Outline each Plasmodium ovale-infected red blood cell.
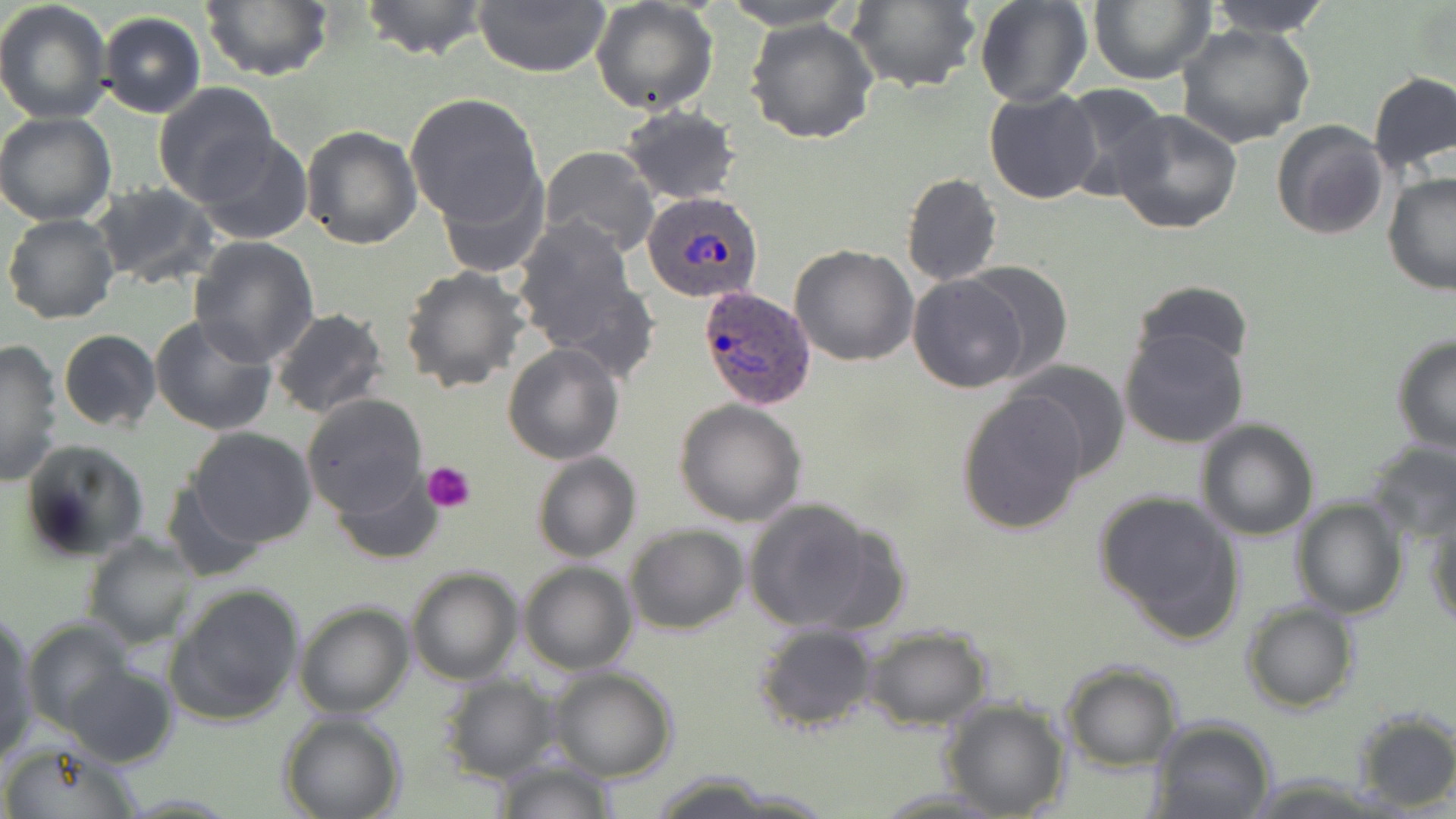

Approximate bounding boxes as [x1, y1, x2, y2] in pixels.
Plasmodium ovale-infected red blood cells: [642, 188, 766, 305], [699, 285, 818, 411].

slide_level_diagnosis: Plasmodium ovale
stain: May-Grünwald-Giemsa
image_size: 1456×819 pixels
modality: optical microscopy
uninfected_red_blood_cell_locations: 'approximate bounding boxes as [x1, y1, x2, y2] in pixels: [0, 0, 114, 125], [358, 0, 492, 60], [471, 0, 611, 76], [716, 0, 861, 29], [846, 0, 981, 93], [974, 0, 1091, 107], [1086, 0, 1215, 86], [1201, 0, 1336, 39], [200, 1, 333, 82], [590, 1, 719, 115], [98, 12, 205, 118], [745, 17, 878, 144], [1175, 23, 1317, 149], [1367, 71, 1456, 178], [153, 81, 279, 203], [1060, 85, 1173, 201], [983, 88, 1103, 204], [406, 95, 545, 228], [620, 106, 740, 204], [1111, 109, 1242, 234], [0, 112, 120, 225], [1271, 119, 1389, 240], [298, 125, 422, 249], [193, 132, 312, 243], [538, 146, 661, 260], [438, 170, 549, 278], [1382, 172, 1456, 297], [901, 173, 1002, 288], [92, 183, 219, 290], [3, 214, 120, 325], [510, 216, 652, 369], [188, 236, 319, 366], [790, 244, 918, 366], [957, 261, 1074, 385], [399, 266, 530, 392], [906, 274, 1030, 393], [1130, 279, 1254, 372], [271, 308, 390, 421], [150, 314, 278, 437], [1118, 328, 1251, 451], [59, 329, 161, 432], [1391, 335, 1456, 454], [0, 339, 64, 487], [502, 343, 625, 465], [1009, 361, 1131, 481], [956, 390, 1089, 536], [300, 393, 428, 517], [675, 398, 807, 526], [1194, 417, 1320, 541], [188, 427, 315, 547], [18, 440, 147, 562], [1367, 441, 1456, 542], [532, 452, 640, 563], [331, 468, 445, 565], [161, 480, 267, 582], [1093, 489, 1246, 641], [742, 498, 891, 635], [1292, 498, 1407, 618], [1426, 505, 1456, 631], [623, 524, 748, 636], [82, 533, 200, 648], [518, 561, 637, 675], [406, 566, 523, 685], [166, 584, 305, 726], [294, 600, 414, 719], [1241, 600, 1360, 714], [0, 616, 38, 765], [22, 618, 134, 733], [753, 624, 879, 734], [863, 624, 993, 729], [1060, 662, 1183, 770], [62, 663, 178, 767], [548, 666, 678, 782], [437, 675, 560, 783], [940, 696, 1071, 818], [1351, 711, 1456, 811], [280, 712, 405, 819], [1150, 716, 1277, 819], [0, 741, 144, 819], [493, 759, 619, 818], [642, 772, 798, 818], [872, 787, 1012, 817]'
field_of_view: one of a larger specimen
preparation: thin blood film
magnification: 1000x
platelet_locations: 'approximate bounding boxes as [x1, y1, x2, y2] in pixels: [422, 462, 476, 513]'